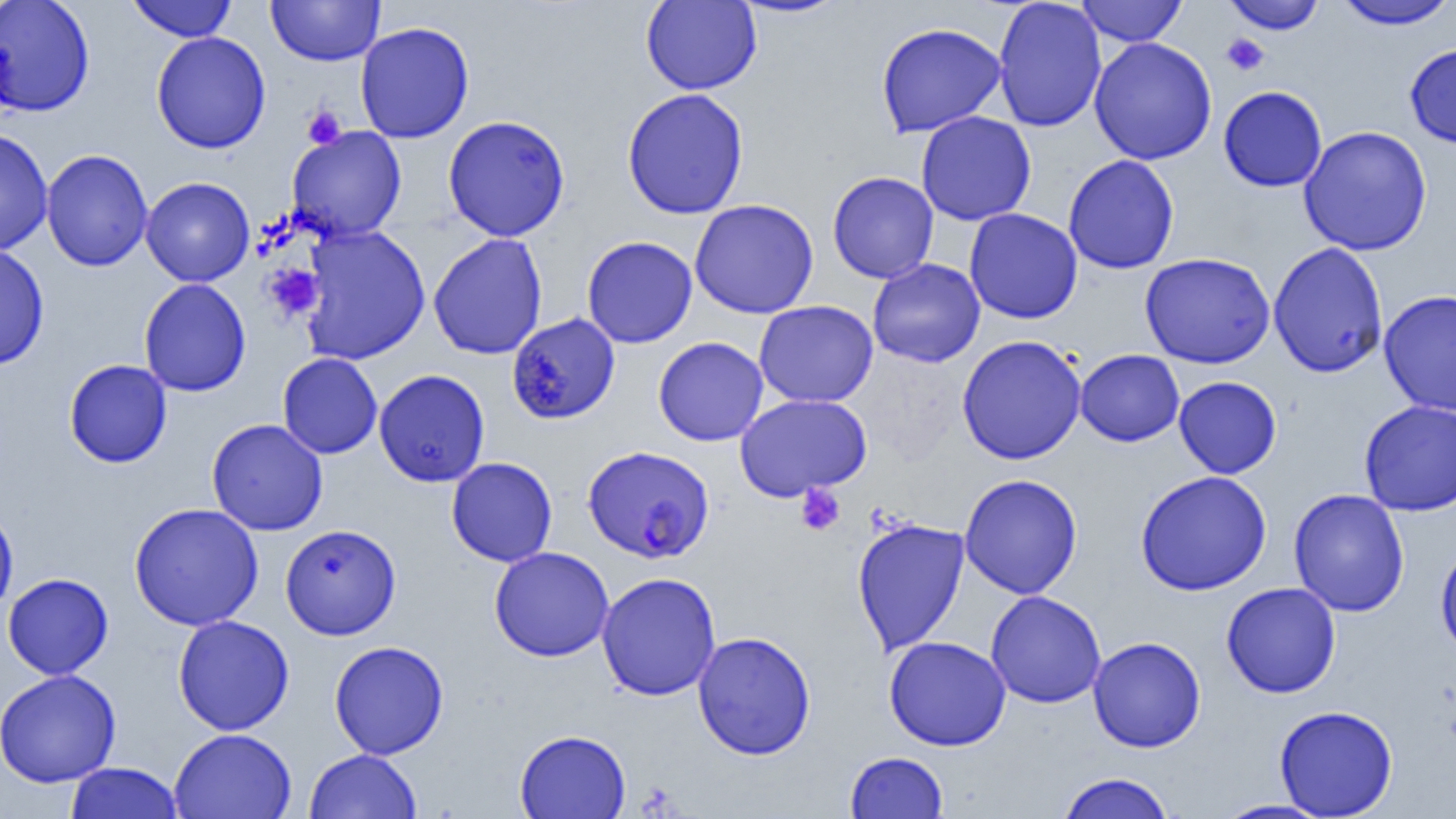
slide-level diagnosis = Plasmodium falciparum
preparation = thin blood smear
magnification = 1000x
Plasmodium falciparum-infected red blood cell locations = approximate bounding boxes as (x1, y1, x2, y2) in pixels: (506, 312, 621, 424), (583, 445, 714, 564)
modality = optical microscopy
uninfected red blood cell locations = approximate bounding boxes as (x1, y1, x2, y2) in pixels: (0, 0, 95, 116), (127, 0, 237, 42), (266, 0, 385, 66), (640, 0, 761, 95), (729, 0, 850, 19), (992, 0, 1106, 133), (1222, 0, 1327, 34), (1076, 1, 1188, 46), (1333, 1, 1456, 30), (355, 21, 475, 143), (876, 22, 1007, 138), (151, 32, 271, 153), (1089, 37, 1217, 165), (1405, 43, 1456, 149), (1218, 86, 1327, 192), (622, 88, 749, 220), (916, 111, 1037, 226), (442, 115, 570, 241), (1298, 125, 1432, 256), (285, 126, 407, 242), (0, 127, 53, 256), (40, 149, 153, 271), (1063, 154, 1179, 274), (827, 171, 939, 283), (140, 177, 255, 287), (689, 199, 819, 319), (964, 208, 1082, 324), (299, 225, 431, 366), (428, 233, 548, 360), (582, 235, 698, 348), (1268, 242, 1389, 378), (0, 243, 50, 370), (1139, 252, 1275, 369), (867, 259, 985, 368), (138, 278, 251, 396), (1378, 290, 1456, 416), (754, 300, 878, 407), (956, 335, 1087, 465), (653, 336, 769, 446), (1075, 349, 1184, 447), (277, 353, 382, 459), (63, 359, 172, 468), (373, 369, 490, 487), (1173, 376, 1282, 478), (734, 393, 872, 500), (1359, 399, 1456, 516), (207, 418, 328, 536), (446, 457, 558, 567), (1135, 470, 1272, 596), (959, 474, 1083, 599), (1288, 488, 1410, 617), (129, 502, 264, 631), (0, 507, 19, 618), (851, 518, 970, 656), (280, 523, 402, 640), (1435, 543, 1456, 661), (488, 546, 614, 662), (596, 572, 722, 701), (2, 573, 113, 680), (1222, 582, 1341, 698), (985, 590, 1106, 708), (172, 615, 294, 735), (692, 631, 816, 760), (884, 635, 1011, 751), (1087, 636, 1206, 752), (329, 640, 449, 760), (0, 669, 121, 788), (1274, 704, 1398, 818), (169, 728, 296, 819), (514, 729, 630, 819), (304, 749, 422, 819), (845, 751, 948, 818), (64, 762, 183, 819), (1056, 772, 1176, 819), (1215, 799, 1333, 818)
platelet locations = approximate bounding boxes as (x1, y1, x2, y2) in pixels: (1221, 33, 1270, 76), (302, 106, 347, 149), (265, 264, 324, 321), (795, 483, 845, 536)
field of view = single
image size = 1456×819 pixels